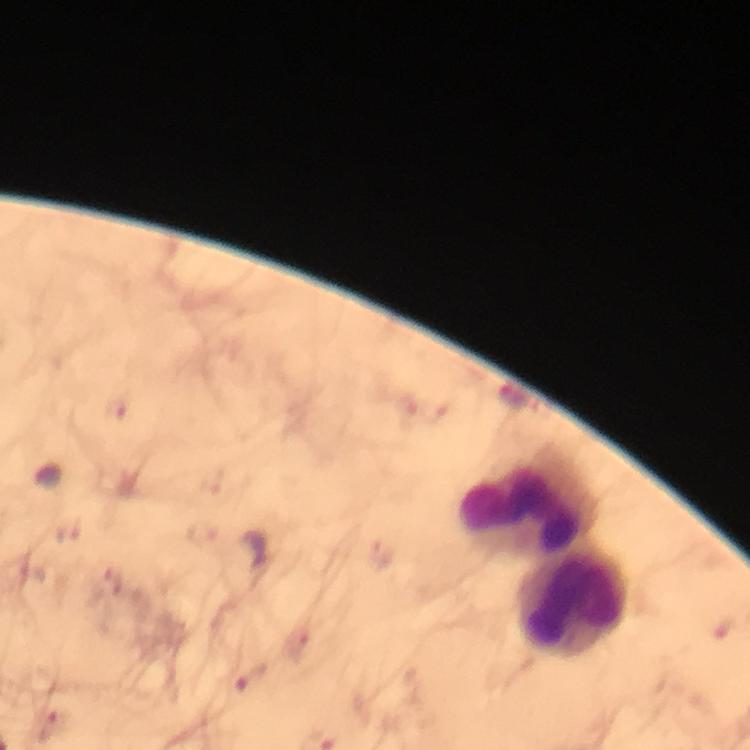
leukocyte locations = approximate centers as {x, y} in pixels: {525, 506}, {573, 606}
stain = Giemsa
image size = 750×750 pixels
context = from a diagnostic examination for malaria
cropped from = one field of view
Plasmodium parasite locations = approximate centers as {x, y} in pixels: {117, 410}, {70, 533}, {254, 552}, {383, 554}, {298, 644}, {252, 677}, {56, 726}
magnification = 100x
immersion oil = applied
preparation = thick smear
capture = smartphone camera through the microscope